State which parasite is depicted.
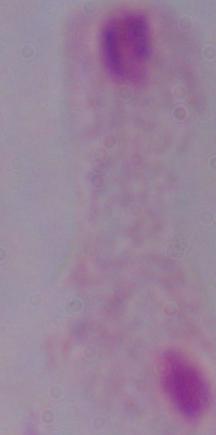

A trichomonad.

Summary:
  - Magnification: 1000x
  - Modality: micrograph